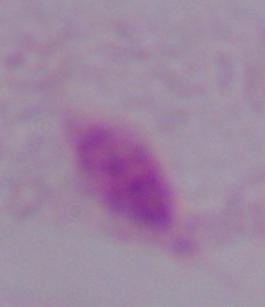
identification: trichomonad
magnification: 1000x
modality: photomicrograph